Describe the morphology of the red blood cells.
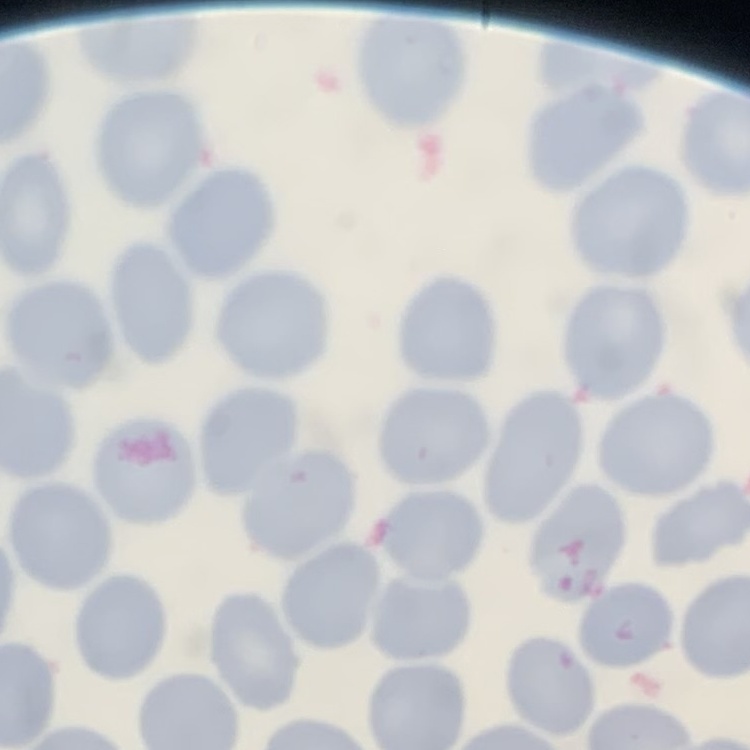
They show no rouleaux formation.

Thin peripheral smear. Square crop of a larger photomicrograph. Stained with either Field's or Giemsa.